Describe the morphology of the erythrocytes.
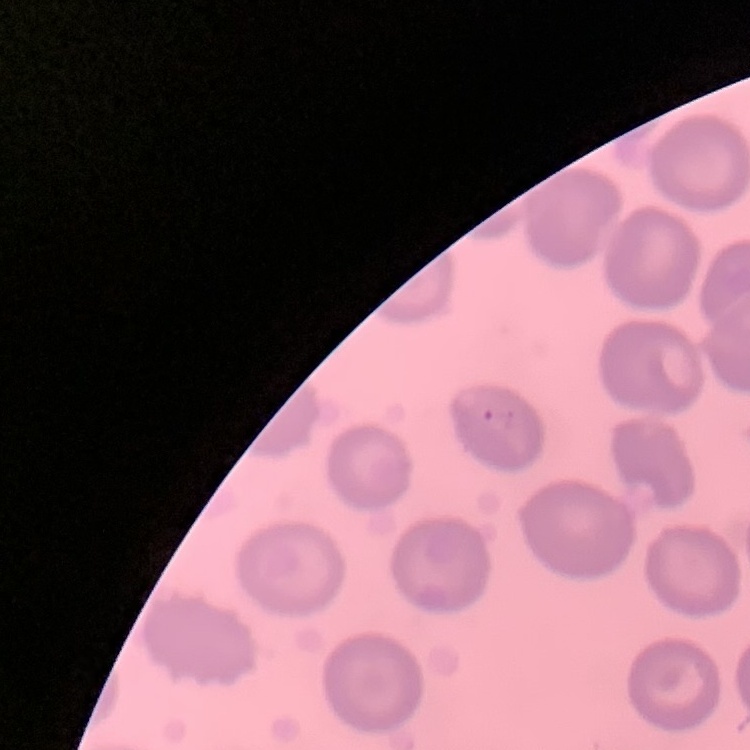

They show no rouleaux formation.

Summary:
  - Stain: Field's or Giemsa
  - Preparation: thin peripheral smear
  - Image type: one tile cut from a larger photomicrograph